Locate every Plasmodium ovale-infected red blood cell.
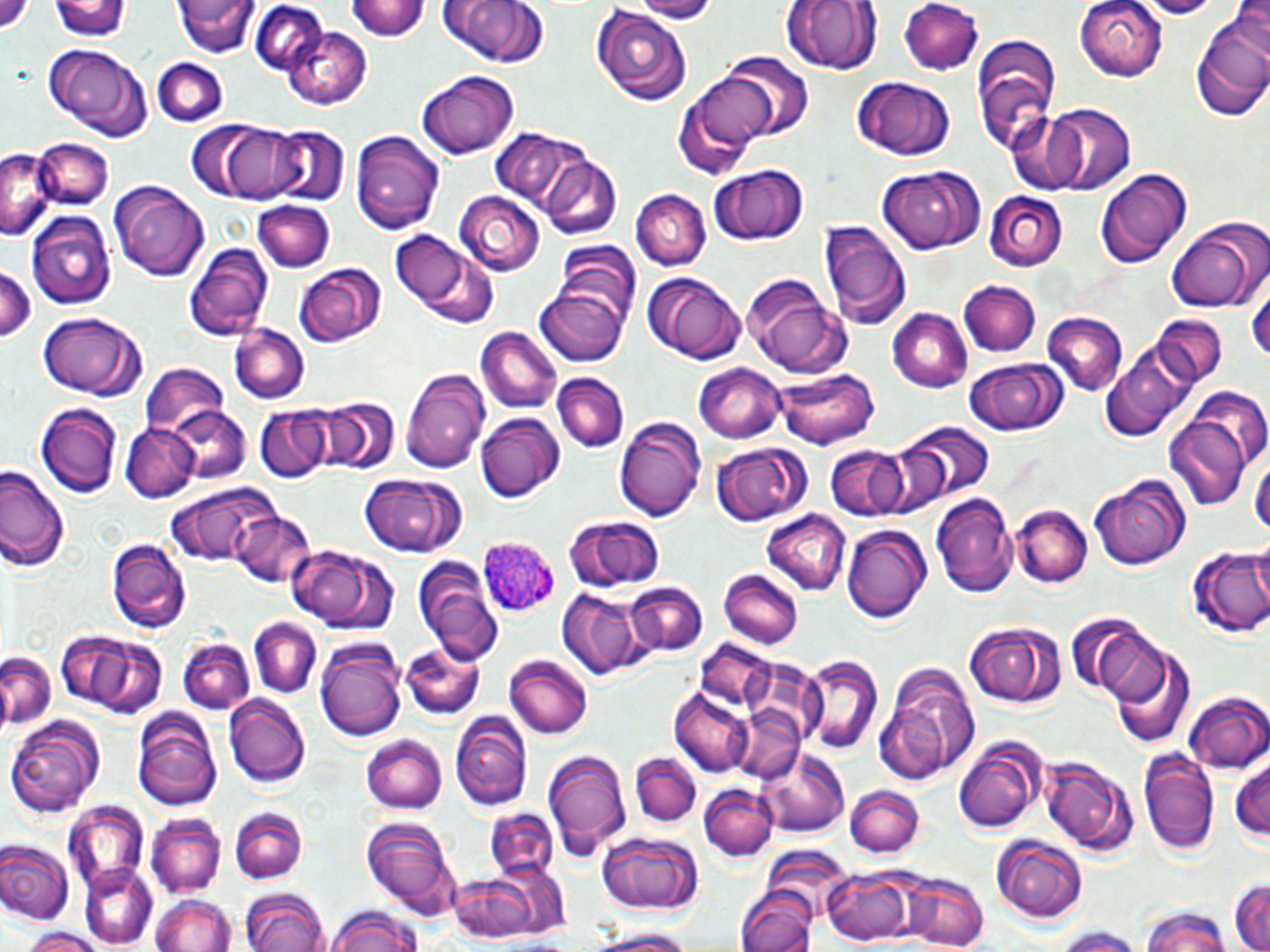

Approximate bounding boxes as named x1/y1/x2/y2 corners in pixels.
Plasmodium ovale-infected red blood cells: (x1=477, y1=534, x2=559, y2=618).

Uninfected red blood cell locations: (x1=175, y1=0, x2=258, y2=57), (x1=346, y1=0, x2=430, y2=42), (x1=436, y1=0, x2=553, y2=69), (x1=628, y1=0, x2=721, y2=21), (x1=1074, y1=0, x2=1168, y2=81), (x1=1132, y1=0, x2=1229, y2=19), (x1=53, y1=1, x2=131, y2=41), (x1=782, y1=1, x2=881, y2=78), (x1=899, y1=1, x2=985, y2=74), (x1=247, y1=4, x2=334, y2=78), (x1=590, y1=4, x2=693, y2=107), (x1=1190, y1=14, x2=1270, y2=121), (x1=282, y1=26, x2=372, y2=110), (x1=970, y1=33, x2=1063, y2=160), (x1=46, y1=44, x2=147, y2=136), (x1=718, y1=53, x2=814, y2=140), (x1=151, y1=57, x2=228, y2=126), (x1=416, y1=70, x2=519, y2=160), (x1=676, y1=73, x2=776, y2=177), (x1=850, y1=75, x2=957, y2=163), (x1=1041, y1=105, x2=1135, y2=196), (x1=210, y1=122, x2=321, y2=204), (x1=264, y1=127, x2=350, y2=210), (x1=351, y1=128, x2=444, y2=234), (x1=487, y1=128, x2=593, y2=220), (x1=33, y1=137, x2=112, y2=208), (x1=0, y1=148, x2=53, y2=238), (x1=538, y1=151, x2=623, y2=239), (x1=703, y1=163, x2=812, y2=248), (x1=874, y1=164, x2=985, y2=255), (x1=1093, y1=166, x2=1193, y2=267), (x1=108, y1=181, x2=212, y2=282), (x1=633, y1=189, x2=710, y2=271), (x1=455, y1=191, x2=546, y2=276), (x1=983, y1=191, x2=1067, y2=272), (x1=251, y1=198, x2=335, y2=272), (x1=26, y1=212, x2=115, y2=311), (x1=1166, y1=214, x2=1270, y2=314), (x1=817, y1=220, x2=911, y2=332), (x1=389, y1=232, x2=497, y2=327), (x1=554, y1=239, x2=642, y2=331), (x1=184, y1=243, x2=273, y2=339), (x1=0, y1=263, x2=42, y2=346), (x1=296, y1=264, x2=386, y2=348), (x1=641, y1=271, x2=747, y2=366), (x1=1249, y1=271, x2=1270, y2=371), (x1=739, y1=276, x2=852, y2=378), (x1=959, y1=280, x2=1042, y2=357), (x1=534, y1=286, x2=627, y2=367), (x1=887, y1=308, x2=972, y2=393), (x1=37, y1=314, x2=144, y2=400), (x1=1042, y1=314, x2=1128, y2=397), (x1=1154, y1=315, x2=1225, y2=387), (x1=230, y1=325, x2=309, y2=404), (x1=474, y1=329, x2=560, y2=416), (x1=1099, y1=349, x2=1193, y2=445), (x1=964, y1=358, x2=1068, y2=437), (x1=695, y1=363, x2=785, y2=443), (x1=138, y1=366, x2=231, y2=440), (x1=775, y1=366, x2=879, y2=449), (x1=400, y1=368, x2=492, y2=474), (x1=553, y1=371, x2=629, y2=453), (x1=320, y1=398, x2=401, y2=476), (x1=37, y1=403, x2=123, y2=501), (x1=1163, y1=405, x2=1257, y2=511), (x1=162, y1=406, x2=253, y2=485), (x1=253, y1=406, x2=332, y2=482), (x1=475, y1=412, x2=565, y2=500), (x1=614, y1=415, x2=706, y2=521), (x1=897, y1=421, x2=993, y2=508), (x1=121, y1=425, x2=197, y2=502), (x1=709, y1=443, x2=811, y2=528), (x1=827, y1=445, x2=907, y2=519), (x1=1249, y1=451, x2=1269, y2=543), (x1=0, y1=463, x2=69, y2=575), (x1=362, y1=475, x2=467, y2=558), (x1=1090, y1=475, x2=1190, y2=570), (x1=165, y1=484, x2=278, y2=569), (x1=932, y1=494, x2=1020, y2=601), (x1=1014, y1=505, x2=1092, y2=588), (x1=231, y1=509, x2=319, y2=590), (x1=763, y1=511, x2=850, y2=594), (x1=565, y1=515, x2=664, y2=593), (x1=843, y1=525, x2=931, y2=626), (x1=106, y1=538, x2=193, y2=634), (x1=1186, y1=545, x2=1270, y2=639), (x1=285, y1=546, x2=401, y2=636), (x1=410, y1=557, x2=501, y2=663), (x1=717, y1=570, x2=803, y2=649), (x1=626, y1=580, x2=707, y2=657), (x1=562, y1=591, x2=652, y2=678), (x1=249, y1=619, x2=321, y2=698), (x1=1074, y1=619, x2=1167, y2=701), (x1=962, y1=620, x2=1067, y2=710), (x1=77, y1=633, x2=169, y2=718), (x1=315, y1=637, x2=405, y2=741), (x1=180, y1=640, x2=254, y2=714), (x1=399, y1=641, x2=488, y2=719), (x1=0, y1=652, x2=59, y2=730), (x1=1113, y1=653, x2=1194, y2=748), (x1=798, y1=655, x2=881, y2=753), (x1=505, y1=656, x2=593, y2=739), (x1=874, y1=660, x2=980, y2=785), (x1=668, y1=691, x2=754, y2=778), (x1=1185, y1=693, x2=1270, y2=773), (x1=223, y1=695, x2=310, y2=788), (x1=131, y1=707, x2=223, y2=809), (x1=452, y1=712, x2=531, y2=812), (x1=6, y1=714, x2=104, y2=818), (x1=360, y1=734, x2=448, y2=816), (x1=953, y1=740, x2=1041, y2=833), (x1=1137, y1=747, x2=1220, y2=858), (x1=542, y1=748, x2=633, y2=859), (x1=758, y1=748, x2=849, y2=836), (x1=630, y1=753, x2=701, y2=824), (x1=1041, y1=755, x2=1135, y2=856), (x1=1229, y1=758, x2=1270, y2=846), (x1=846, y1=783, x2=922, y2=858), (x1=699, y1=785, x2=778, y2=862), (x1=61, y1=803, x2=148, y2=899), (x1=231, y1=807, x2=306, y2=884), (x1=482, y1=809, x2=558, y2=883), (x1=146, y1=814, x2=224, y2=898), (x1=359, y1=817, x2=459, y2=920), (x1=993, y1=832, x2=1089, y2=923), (x1=599, y1=834, x2=705, y2=915), (x1=0, y1=842, x2=72, y2=925), (x1=78, y1=862, x2=157, y2=949), (x1=441, y1=868, x2=563, y2=945), (x1=821, y1=868, x2=919, y2=945), (x1=900, y1=873, x2=988, y2=952), (x1=1229, y1=876, x2=1269, y2=952), (x1=736, y1=887, x2=817, y2=952), (x1=243, y1=890, x2=327, y2=952), (x1=152, y1=893, x2=236, y2=952), (x1=1138, y1=907, x2=1232, y2=952), (x1=325, y1=908, x2=425, y2=952), (x1=1050, y1=927, x2=1145, y2=952), (x1=19, y1=928, x2=106, y2=952), (x1=582, y1=929, x2=704, y2=952). Slide-level diagnosis: Plasmodium ovale. Image is 1270×952 pixels. May-Grünwald-Giemsa stain. Thin blood film. One field of a larger specimen. 1000x magnification. Optical microscopy.